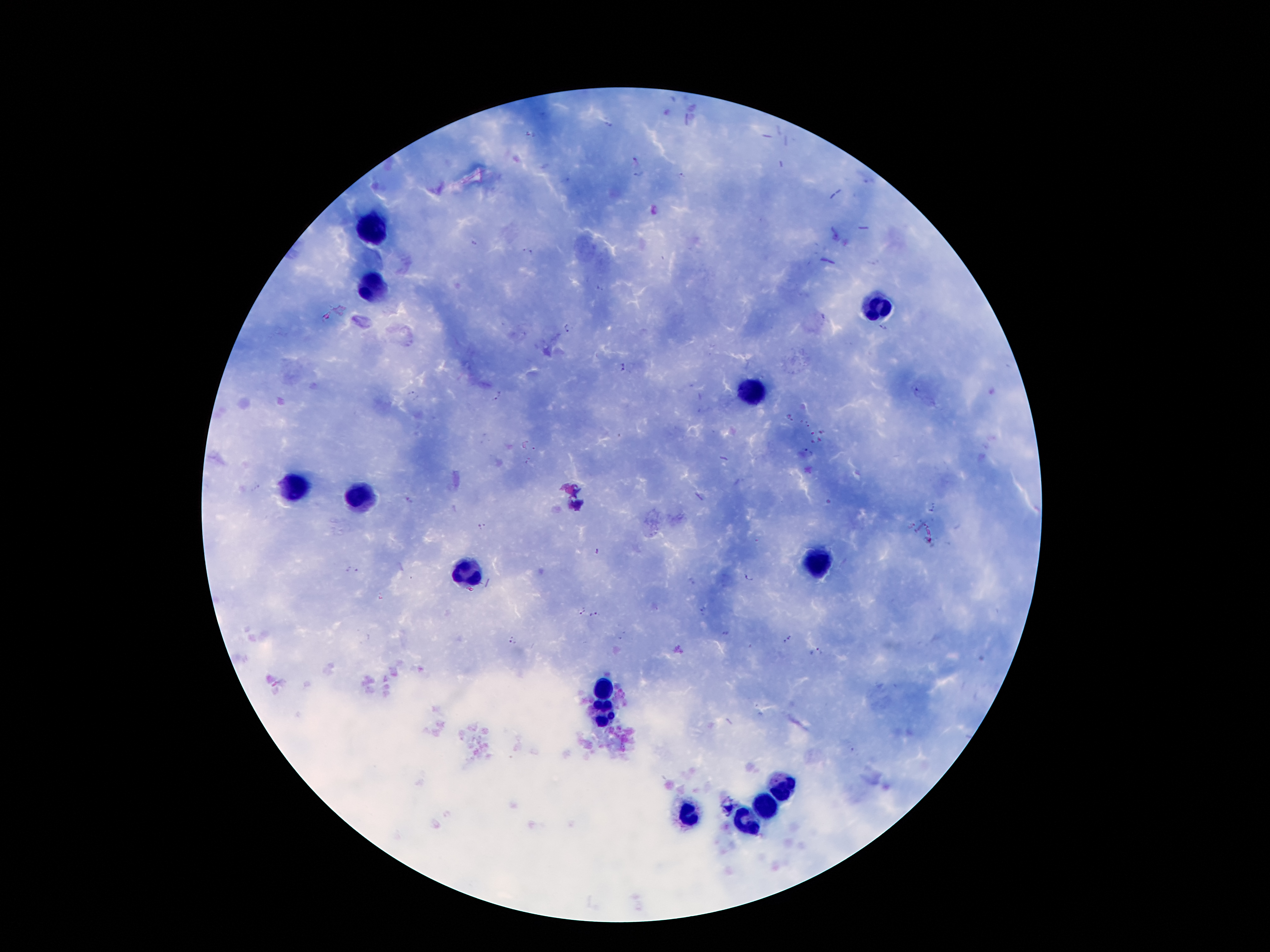

Approximate centers as (x, y) in pixels.
Summary:
  - Malaria parasite locations: (608, 123), (637, 161), (638, 175), (682, 176), (655, 211), (474, 242), (524, 250), (532, 252), (600, 289), (567, 327), (883, 328), (624, 367), (916, 390), (413, 395), (497, 396), (808, 424), (804, 450), (256, 488), (407, 500), (930, 511), (911, 524), (483, 527), (596, 552), (353, 571), (749, 578), (580, 611), (702, 613), (594, 615), (725, 633), (788, 639), (513, 640), (814, 653)
  - Leukocyte locations: (375, 227), (374, 290), (876, 308), (754, 392), (293, 488), (356, 497), (815, 561), (468, 574), (606, 686), (604, 713), (786, 786), (767, 811), (690, 817), (752, 824)
  - Magnification: 100x
  - Preparation: thick blood smear
  - Capture: smartphone through the microscope eyepiece
  - Stain: Giemsa
  - Field of view: single
  - Image size: 1270×952 pixels
  - Patient malaria status: positive for Plasmodium falciparum